Name the blood parasite species.
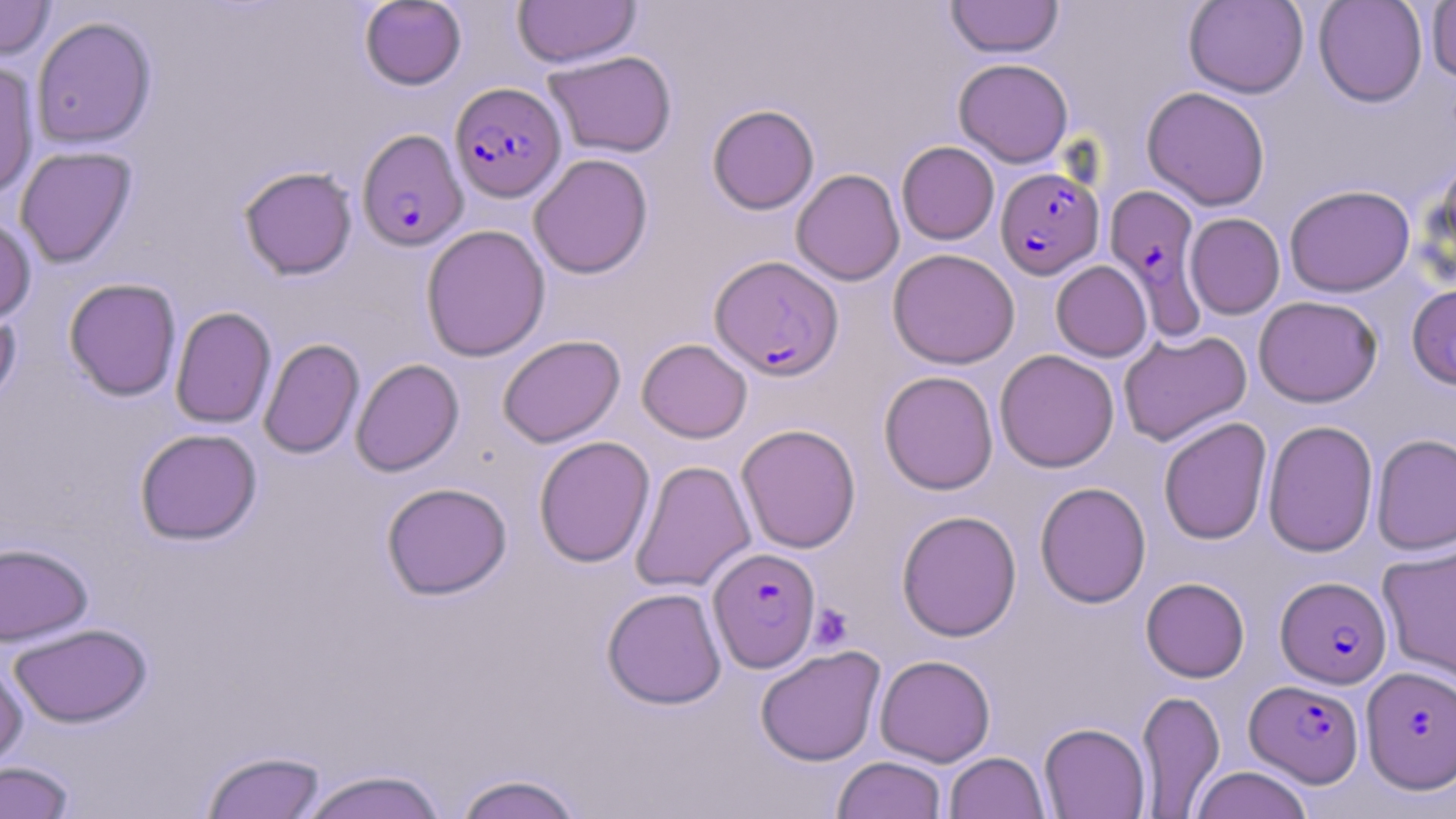

Plasmodium falciparum.

Summary:
  - Coordinate format: approximate bounding boxes as (x1, y1, x2, y2) in pixels
  - Plasmodium falciparum-infected red blood cell locations: (450, 82, 566, 202), (357, 129, 468, 251), (996, 167, 1104, 278), (1105, 184, 1206, 337), (709, 255, 843, 380), (709, 547, 821, 672), (1276, 576, 1392, 688), (1361, 665, 1455, 793), (1245, 679, 1364, 787)
  - Uninfected red blood cell locations: (0, 0, 55, 60), (513, 0, 641, 67), (945, 0, 1064, 58), (1183, 0, 1309, 98), (1313, 0, 1428, 107), (1426, 0, 1456, 84), (359, 1, 467, 90), (31, 16, 157, 149), (543, 50, 677, 158), (953, 58, 1073, 167), (0, 61, 40, 201), (1142, 86, 1271, 210), (707, 104, 819, 214), (897, 141, 999, 245), (15, 146, 137, 267), (528, 153, 653, 279), (1431, 155, 1456, 275), (238, 166, 358, 280), (791, 169, 904, 286), (1284, 184, 1415, 297), (1185, 213, 1285, 319), (0, 215, 37, 324), (421, 224, 551, 361), (888, 248, 1020, 369), (1051, 260, 1152, 361), (63, 278, 182, 401), (1407, 284, 1456, 389), (1253, 295, 1382, 407), (0, 304, 21, 413), (170, 307, 276, 429), (1118, 329, 1252, 446), (497, 334, 625, 448), (259, 338, 364, 459), (637, 338, 752, 443), (994, 349, 1119, 473), (350, 358, 464, 476), (879, 370, 998, 495), (1158, 417, 1272, 545), (1262, 419, 1378, 557), (736, 423, 861, 553), (134, 428, 263, 545), (1371, 433, 1456, 556), (534, 436, 655, 568), (630, 460, 755, 593), (1035, 481, 1151, 608), (381, 482, 512, 600), (896, 510, 1022, 642), (0, 543, 93, 645), (1378, 545, 1456, 683), (1141, 577, 1250, 682), (602, 587, 727, 709), (9, 623, 152, 728), (755, 645, 886, 766), (874, 654, 996, 766), (0, 660, 28, 773), (1136, 689, 1225, 818), (1038, 722, 1150, 818), (201, 749, 326, 819), (945, 752, 1050, 819), (832, 756, 947, 819), (0, 761, 75, 819), (1190, 766, 1314, 819), (297, 769, 449, 819), (452, 772, 587, 819)
  - Platelet locations: (809, 604, 853, 651)
  - Field of view: one of a larger specimen
  - Stain: May-Grünwald-Giemsa
  - Image size: 1456×819 pixels
  - Magnification: 1000x
  - Modality: light microscopy
  - Preparation: thin blood film